Locate every P. falciparum parasite and identify its life-cycle stage.
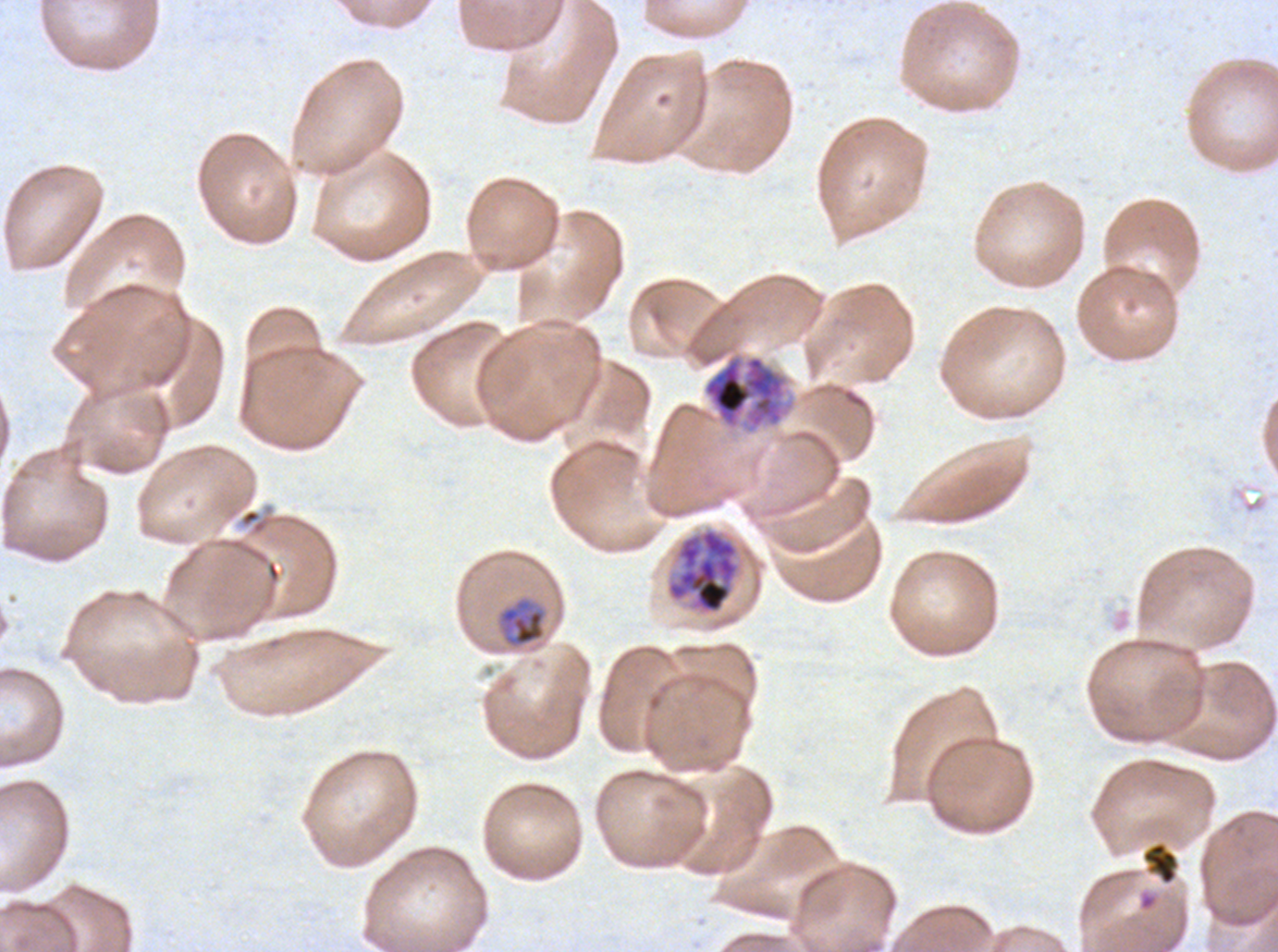

Approximate bounding rectangles given as corner coordinates in pixels from the top-left.
Mid trophozoites: (x1=498, y1=598, x2=546, y2=647).
Early schizonts: (x1=702, y1=351, x2=796, y2=435).
Late schizonts: (x1=666, y1=528, x2=740, y2=615).
No rings, late-ring/early-trophozoite forms, late trophozoites, segmenters, or gametocytes observed.

Summary:
  - Debris locations: (x1=240, y1=508, x2=261, y2=527), (x1=1140, y1=841, x2=1180, y2=885)
  - Image size: 1278×952 pixels
  - Stain: Giemsa
  - Life-cycle stages observed: mid trophozoite, early schizont, late schizont
  - Preparation: thin blood smear
  - Field of view: sub-image separated from a larger composite
  - Specimen: P. falciparum cultured ex vivo for 24 to 48 hours, from a patient in The Gambia